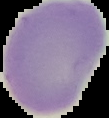
image size = 109×118 pixels
preparation = thin blood smear
image type = segmented cell region on a black background
result = no Plasmodium parasites detected